Point out each Plasmodium parasite.
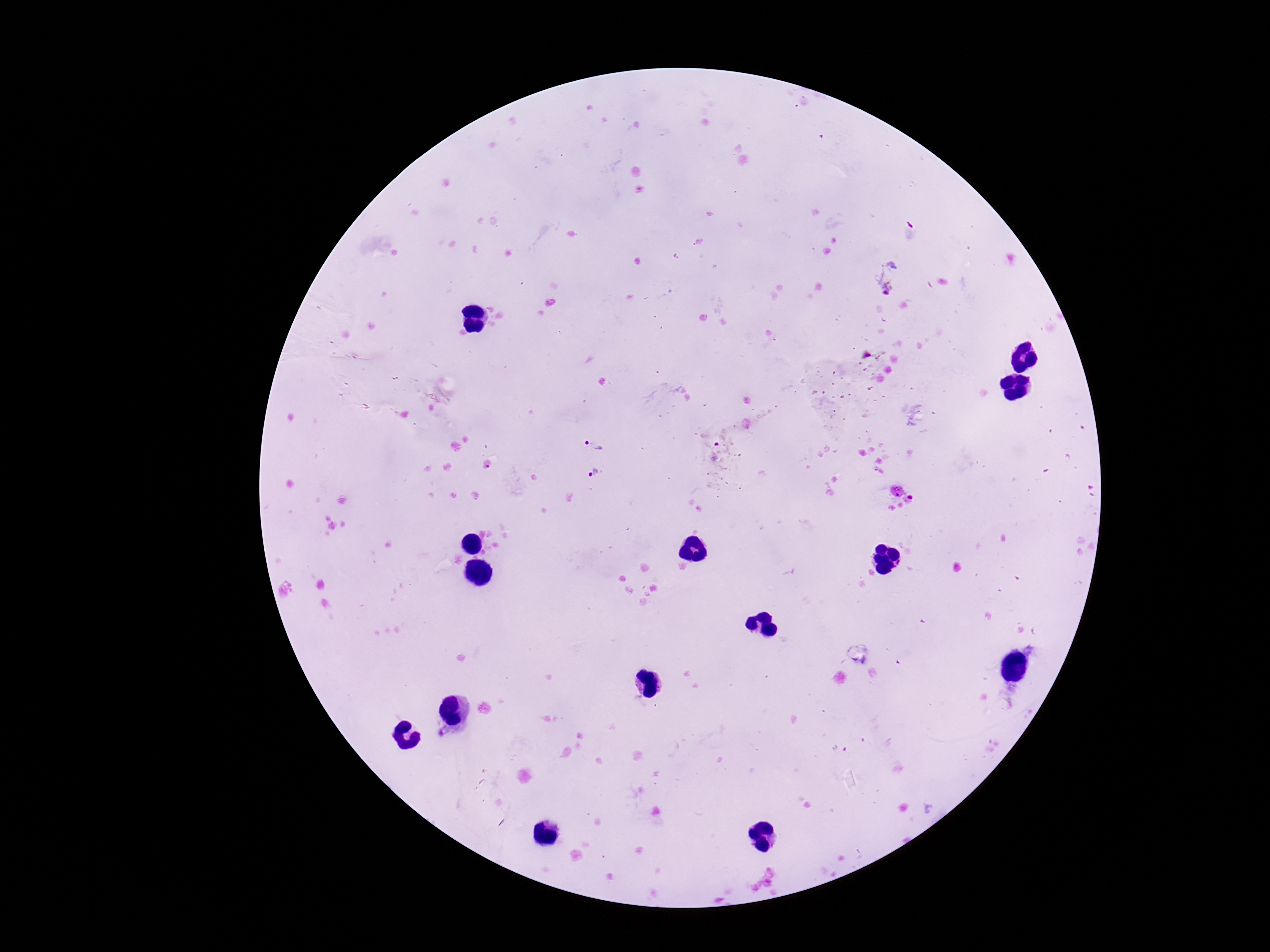

Approximate object centers, in pixels from the top-left corner.
Plasmodium parasites: (x=889, y=278), (x=595, y=441), (x=718, y=444), (x=597, y=473).

Giemsa stain. 100x magnification. Smartphone photograph taken through the microscope eyepiece. Thick blood smear. Image is 1270×952 pixels. One field from this slide. Patient malaria status: positive.